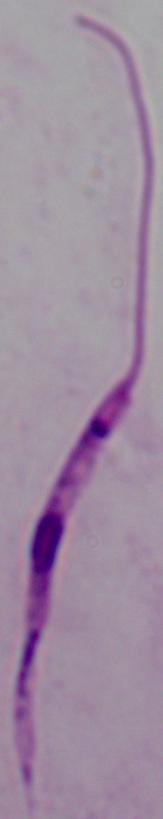

Summary:
  - Modality: photomicrograph
  - Identification: Leishmania
  - Magnification: 1000x